Report the malaria status of this cell.
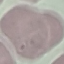

It is uninfected.

Automatically extracted cell patch, resized to 64 × 64 pixels. Acquired by smartphone through the microscope eyepiece. Giemsa-stained preparation. Thin blood film.